Describe the morphology of the erythrocytes.
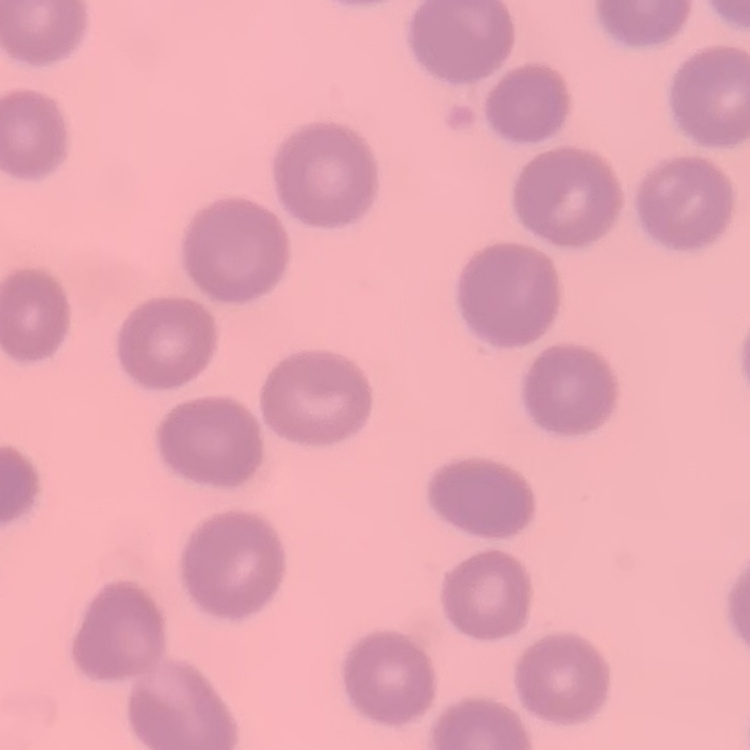
They show no rouleaux formation.

Summary:
  - Image type: one tile cut from a larger photomicrograph
  - Stain: Field's or Giemsa
  - Preparation: thin blood smear